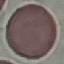

Summary:
  - Malaria status: uninfected
  - Capture: smartphone through the microscope eyepiece
  - Preparation: thin blood smear
  - Stain: Giemsa
  - Image type: cell patch, automatically extracted from a larger field of view and resized to 64 × 64 pixels